Identify the parasite.
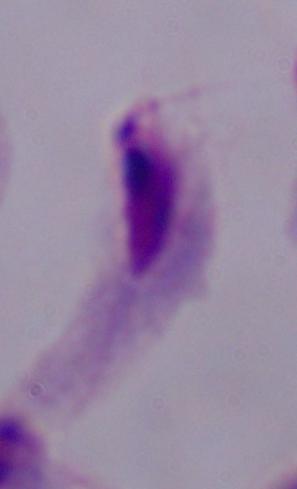
A trichomonad.

Micrograph. 1000x magnification.